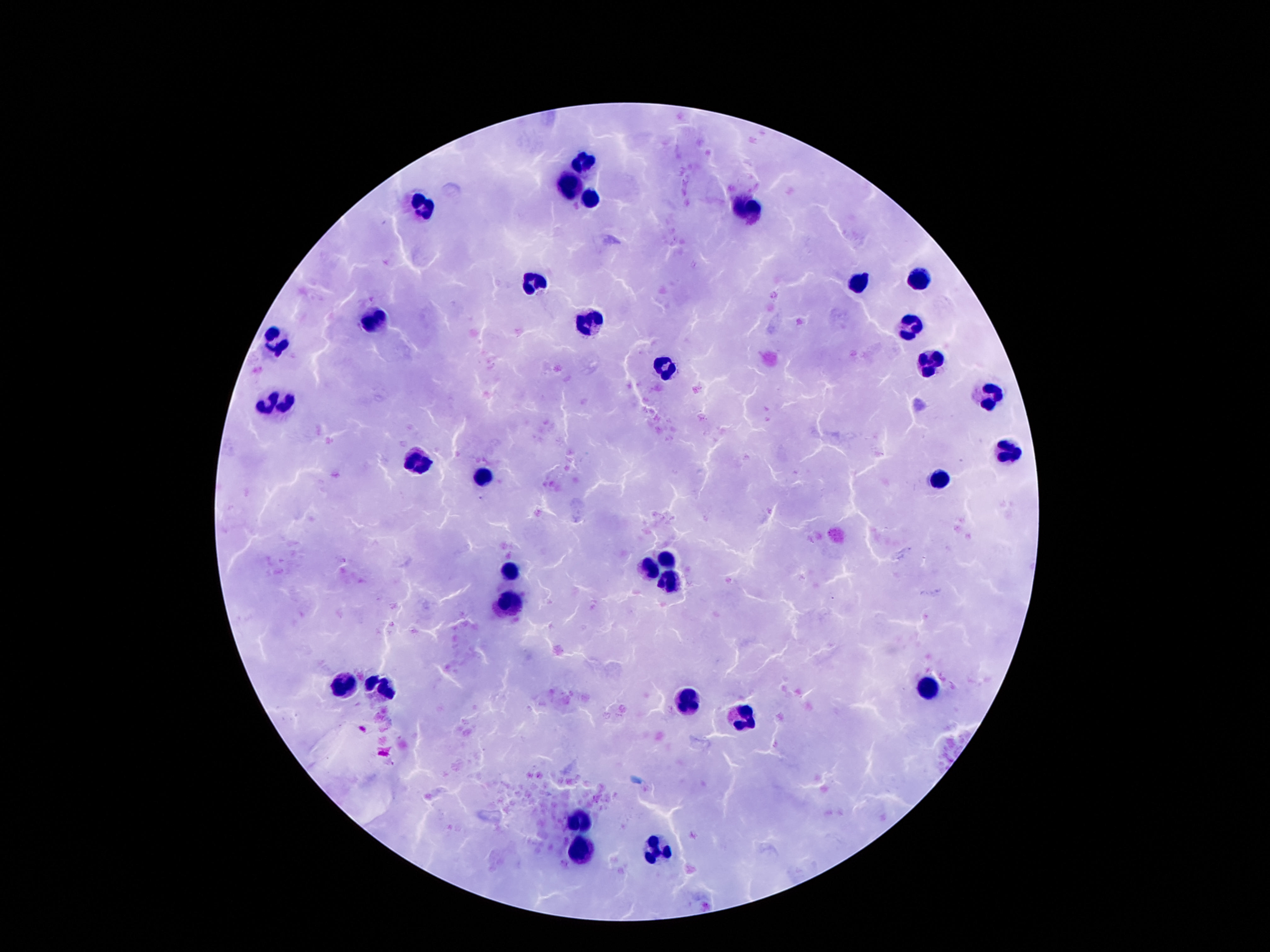
Approximate centers as (x, y) in pixels.
Summary:
  - Leukocyte locations: (583, 161), (570, 184), (593, 199), (421, 204), (749, 212), (919, 277), (529, 279), (858, 279), (374, 320), (589, 322), (912, 328), (279, 342), (927, 360), (665, 368), (990, 393), (264, 402), (285, 404), (1007, 456), (419, 462), (479, 477), (940, 479), (667, 562), (511, 568), (647, 570), (669, 581), (507, 602), (341, 684), (923, 686), (380, 688), (690, 702), (740, 714), (578, 821), (656, 846), (580, 850)
  - Capture: smartphone camera through the microscope eyepiece
  - Magnification: 100x
  - Field of view: one from this slide
  - Image size: 1270×952 pixels
  - Stain: Giemsa
  - Preparation: thick blood smear
  - Patient malaria status: not infected